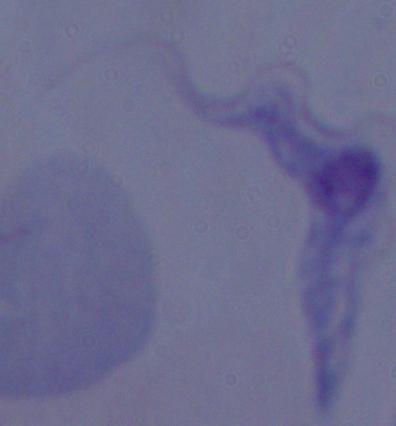
Summary:
  - Identification: trypanosome
  - Modality: micrograph
  - Magnification: 1000x